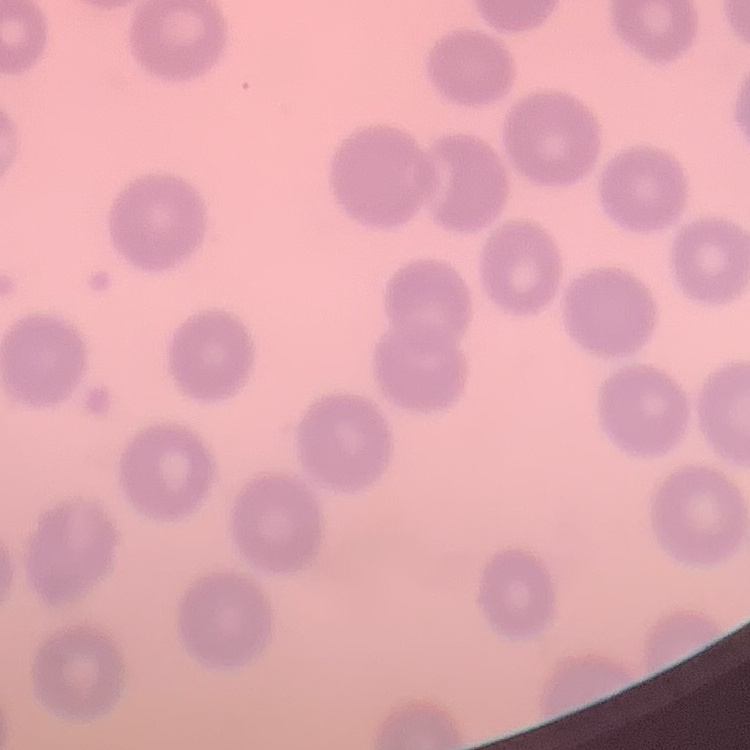

The erythrocytes show no rouleaux formation. One tile cut from a larger photomicrograph. Field's or Giemsa stain. Thin peripheral smear.